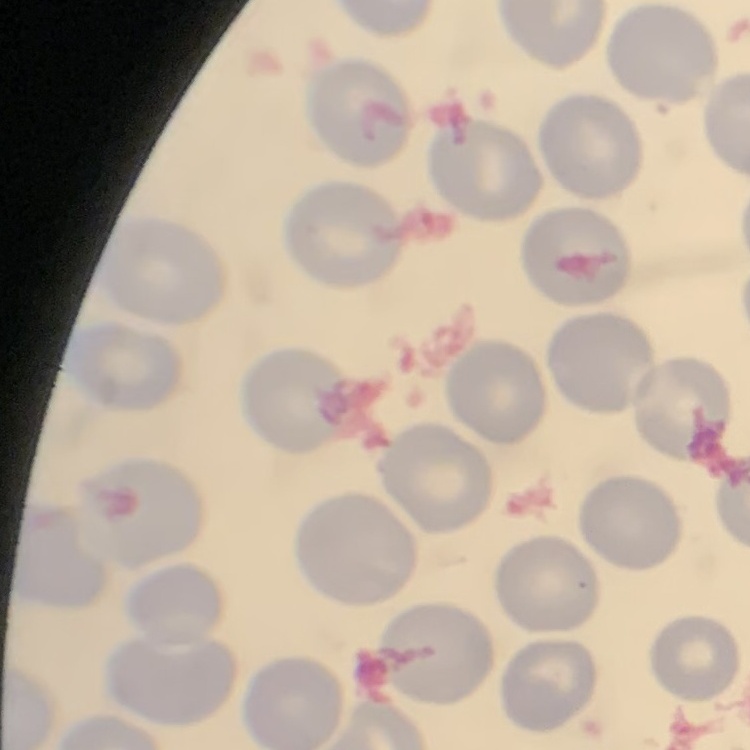
red blood cell morphology = no rouleaux formation
preparation = thin blood film
stain = Field's or Giemsa
image type = one tile cut from a larger photomicrograph